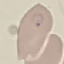
Summary:
  - Result: malaria parasites detected
  - Capture: smartphone through the microscope eyepiece
  - Stain: Giemsa
  - Image type: automatically extracted cell patch, resized to 64 × 64 pixels
  - Preparation: thin blood film